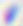 Toxoplasma gondii is shown. Captured at 400x magnification. Photomicrograph.